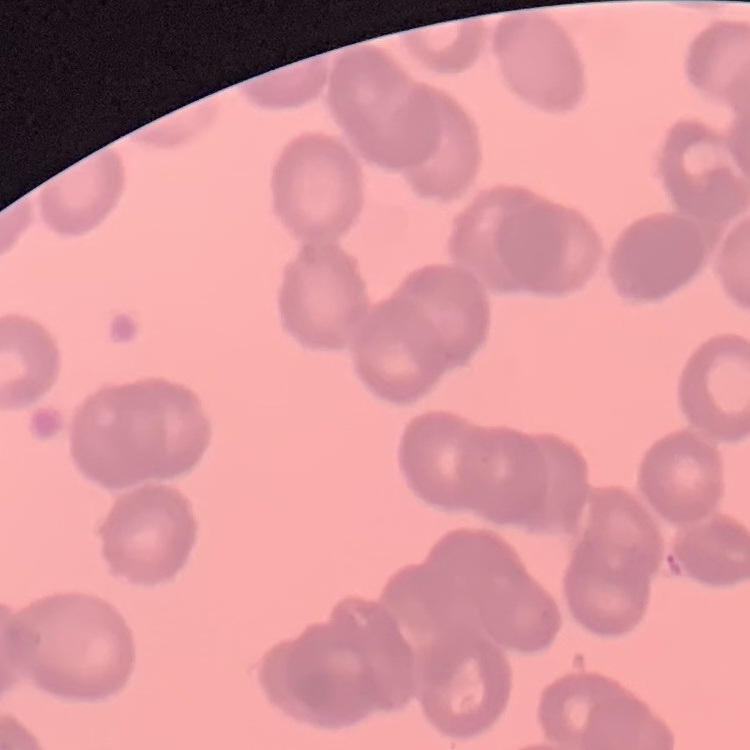
The erythrocytes show rouleaux formation. Stained with either Field's or Giemsa. Square crop of a larger photomicrograph. Thin blood film.